Locate every blood parasite and identify its species.
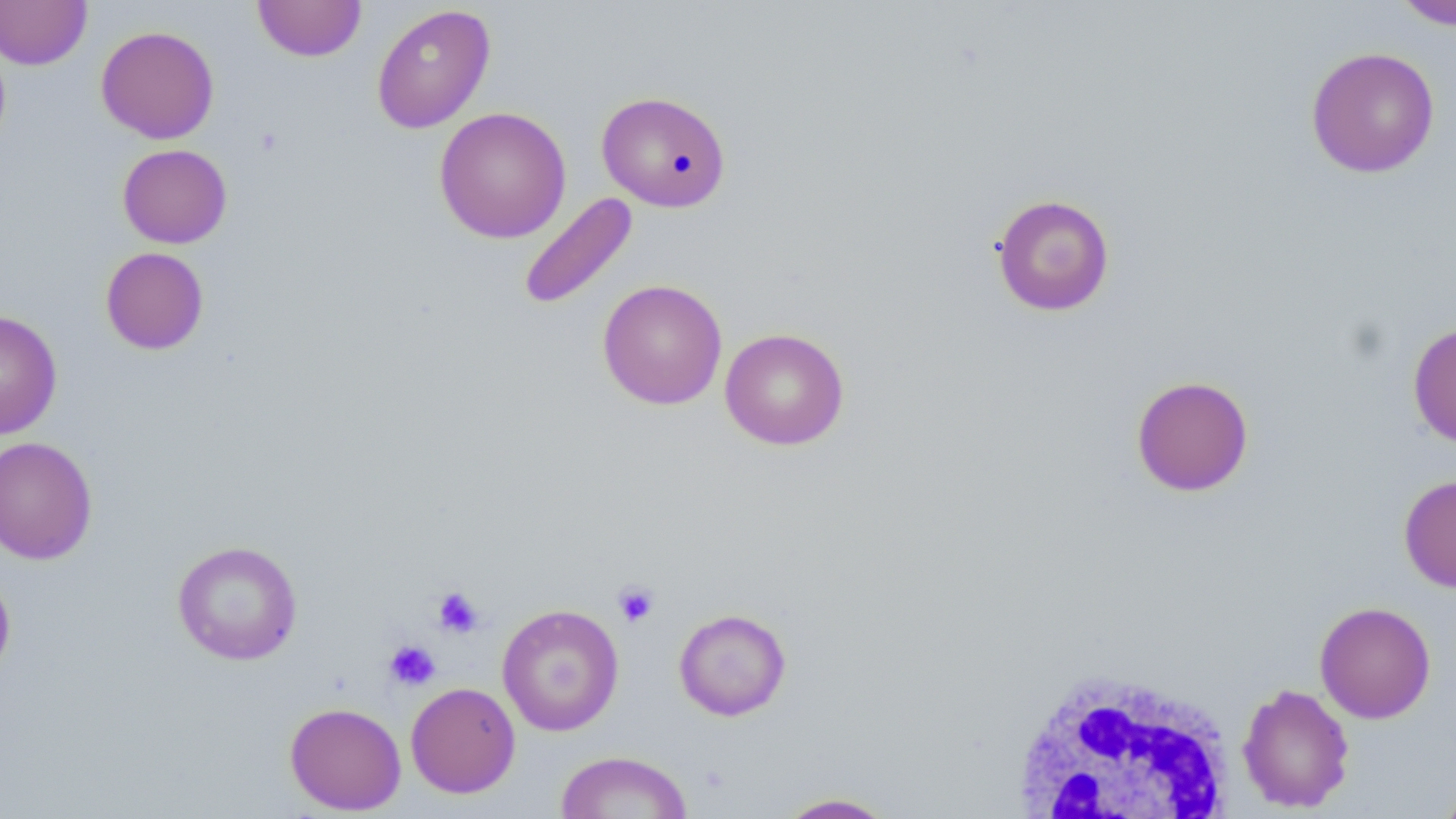
No blood parasites seen.

slide-level diagnosis = no evidence of blood parasites
field of view = single
image size = 1456×819 pixels
platelet locations = approximate bounding boxes as named x1/y1/x2/y2 corners in pixels: (x1=612, y1=581, x2=660, y2=628), (x1=431, y1=585, x2=485, y2=638), (x1=383, y1=639, x2=441, y2=691)
magnification = 1000x
stain = May-Grünwald-Giemsa
uninfected red blood cell locations = approximate bounding boxes as named x1/y1/x2/y2 corners in pixels: (x1=252, y1=0, x2=367, y2=62), (x1=1391, y1=0, x2=1456, y2=30), (x1=0, y1=1, x2=92, y2=69), (x1=371, y1=4, x2=495, y2=134), (x1=96, y1=25, x2=219, y2=143), (x1=1305, y1=46, x2=1440, y2=178), (x1=596, y1=90, x2=731, y2=212), (x1=434, y1=106, x2=572, y2=244), (x1=117, y1=143, x2=232, y2=249), (x1=518, y1=191, x2=639, y2=311), (x1=991, y1=193, x2=1115, y2=316), (x1=100, y1=247, x2=209, y2=355), (x1=597, y1=279, x2=728, y2=410), (x1=0, y1=310, x2=62, y2=439), (x1=1407, y1=321, x2=1456, y2=450), (x1=719, y1=328, x2=850, y2=450), (x1=1131, y1=375, x2=1254, y2=497), (x1=0, y1=436, x2=98, y2=565), (x1=1399, y1=473, x2=1456, y2=593), (x1=171, y1=540, x2=303, y2=665), (x1=0, y1=568, x2=16, y2=680), (x1=1314, y1=601, x2=1436, y2=724), (x1=497, y1=604, x2=624, y2=736), (x1=673, y1=608, x2=792, y2=721), (x1=406, y1=682, x2=520, y2=798), (x1=1237, y1=682, x2=1355, y2=813), (x1=285, y1=702, x2=406, y2=815), (x1=554, y1=750, x2=692, y2=819), (x1=1435, y1=776, x2=1456, y2=819), (x1=773, y1=792, x2=900, y2=818)
modality = optical microscopy
white blood cell locations = approximate bounding boxes as named x1/y1/x2/y2 corners in pixels: (x1=1003, y1=668, x2=1237, y2=819)
preparation = thin blood film